Classify this cell by malaria status.
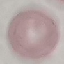
It is uninfected.

Automatically extracted cell patch, resized to 64 × 64 pixels. Photographed with a smartphone camera at the microscope eyepiece. Giemsa-stained preparation. Thin blood smear.